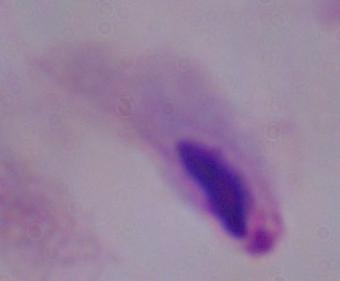 1000x magnification. A trichomonad is shown. Micrograph.